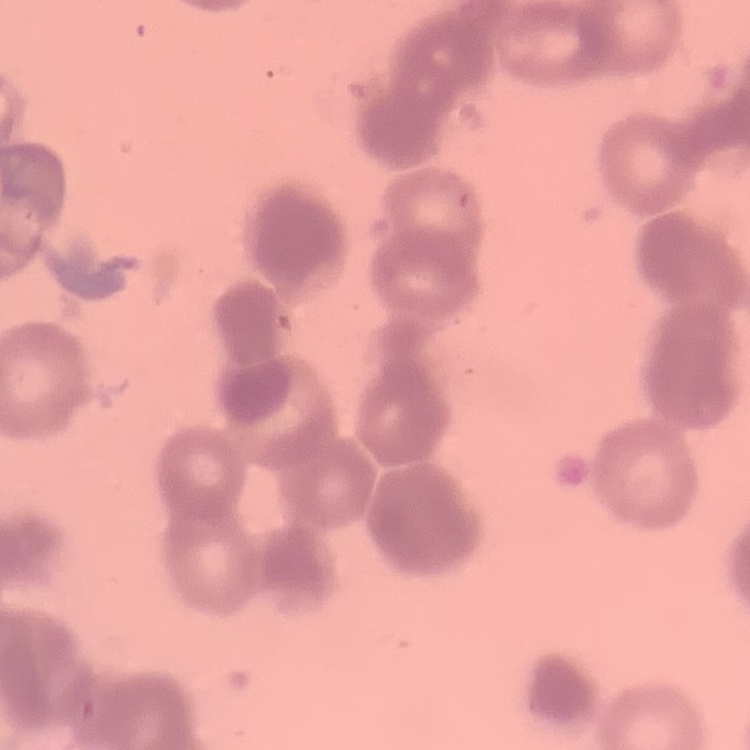

The red blood cells show rouleaux formation. Thin blood smear. Square crop of a larger photomicrograph. Stained with either Field's or Giemsa.